Assess this cell for malaria.
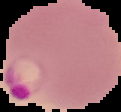

It is parasitized.

Summary:
  - Image type: segmented cell region on a black background
  - Image size: 121×112 pixels
  - Preparation: thin blood film